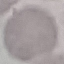
Summary:
  - Result: no malaria parasites seen
  - Preparation: thin blood smear
  - Image type: automatically extracted cell patch, resized to 64 × 64 pixels
  - Capture: smartphone camera at the microscope eyepiece
  - Stain: Giemsa